Locate every leukocyte (white blood cell).
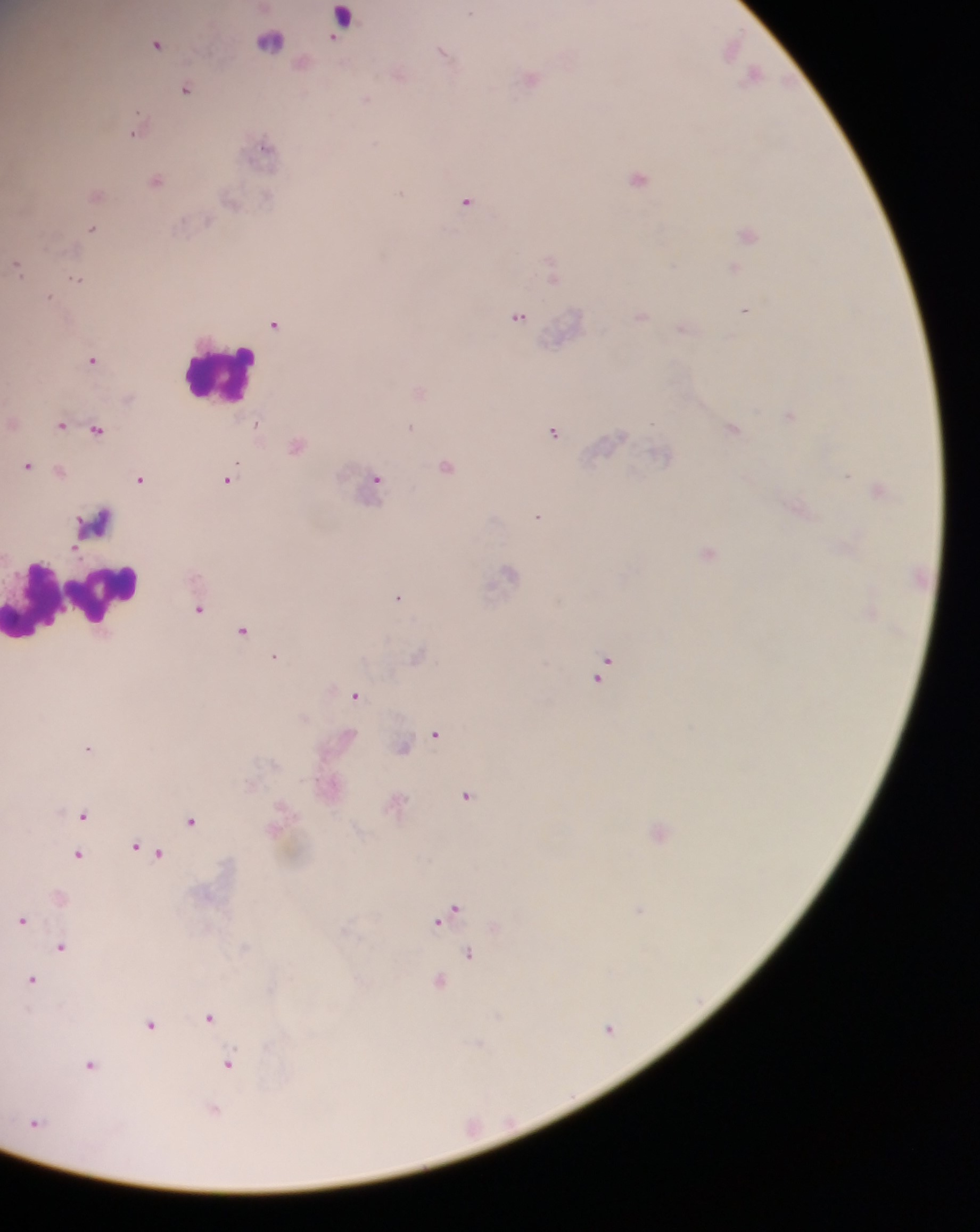
Approximate centers as x y in pixels.
Leukocytes: 220 373; 96 521; 75 599.
One object is labeled both malaria parasite and leukocyte by the source: 341 20.

Malaria parasite locations: 269 41; 157 43; 732 47; 444 53; 399 74; 755 74; 531 76; 187 88; 137 129; 265 146; 637 177; 156 179; 96 194; 466 200; 93 228; 748 233; 18 266; 551 267; 733 267; 78 278; 49 297; 745 310; 642 315; 519 316; 274 324; 683 328; 92 359; 419 391; 789 414; 61 424; 410 427; 733 428; 96 429; 554 430; 295 445; 661 453; 27 465; 446 466; 59 470; 140 478; 227 480; 377 481; 879 489; 799 506; 538 515; 708 552; 508 572; 398 596; 199 608; 243 630; 274 657; 602 666; 356 695; 435 733; 402 746; 88 749; 466 796; 395 803; 83 814; 191 820; 659 831; 141 847; 154 852; 78 853; 453 909; 640 909; 443 917; 23 920; 61 946; 469 952; 32 979; 440 981; 209 1017; 150 1025; 610 1027; 228 1063; 91 1065; 214 1108; 35 1121. Mobile-phone photograph taken through the microscope. Sample from Ghana. Thick blood film. One field of view. Image is 980×1232 pixels.